Give the extent of all Plasmodium ovale-infected red blood cells.
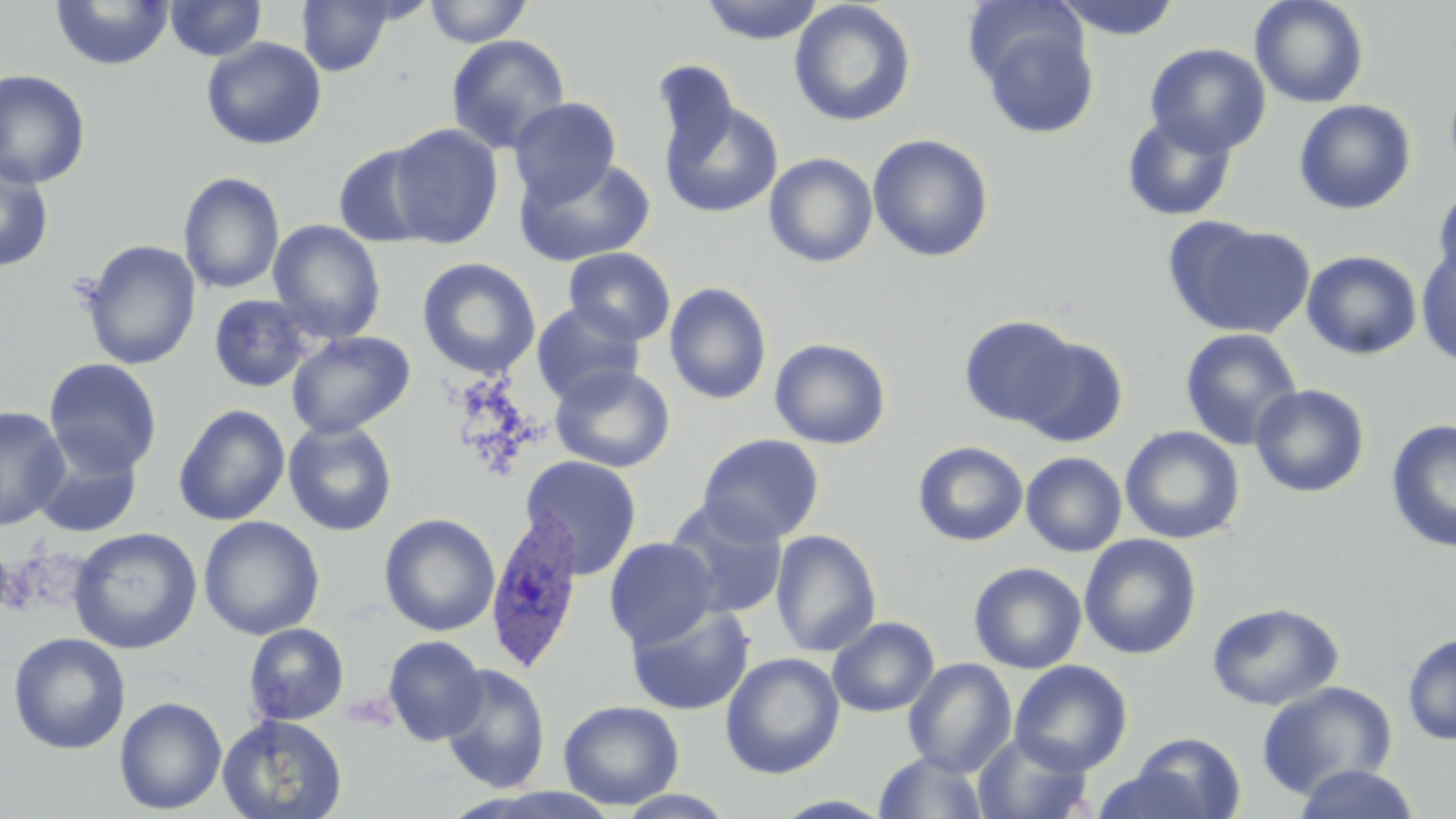
Approximate bounding boxes as [x1, y1, x2, y2] in pixels.
Plasmodium ovale-infected red blood cells: [485, 509, 585, 673].

Summary:
  - Uninfected red blood cell locations: [51, 0, 174, 70], [165, 0, 267, 61], [297, 0, 398, 76], [424, 0, 533, 47], [698, 0, 826, 44], [1052, 0, 1184, 40], [1249, 0, 1370, 109], [789, 1, 916, 127], [976, 16, 1100, 139], [445, 34, 571, 154], [201, 37, 327, 150], [1144, 43, 1272, 156], [650, 58, 742, 169], [0, 69, 92, 189], [508, 97, 621, 205], [659, 98, 783, 219], [1293, 99, 1417, 215], [1121, 113, 1238, 222], [387, 123, 504, 248], [867, 134, 994, 262], [333, 143, 438, 249], [764, 152, 878, 267], [0, 155, 54, 273], [514, 155, 656, 267], [178, 171, 285, 295], [1431, 183, 1456, 297], [1166, 218, 1315, 340], [267, 219, 386, 344], [81, 240, 201, 370], [1416, 246, 1456, 367], [563, 247, 676, 346], [1302, 250, 1422, 360], [417, 258, 541, 378], [664, 282, 772, 405], [208, 294, 314, 393], [531, 301, 645, 405], [958, 315, 1081, 428], [1179, 328, 1303, 450], [286, 330, 415, 439], [1015, 336, 1129, 447], [769, 338, 891, 450], [44, 358, 163, 476], [549, 364, 676, 473], [1249, 383, 1371, 498], [173, 404, 290, 526], [0, 406, 70, 530], [1385, 419, 1456, 553], [283, 420, 398, 537], [1120, 425, 1245, 544], [697, 433, 825, 546], [31, 437, 143, 538], [913, 441, 1028, 546], [1021, 452, 1127, 557], [519, 456, 643, 580], [666, 499, 790, 618], [379, 513, 500, 636], [198, 515, 325, 640], [68, 527, 202, 654], [770, 529, 882, 657], [1079, 534, 1202, 659], [604, 536, 720, 649], [968, 561, 1088, 674], [625, 602, 755, 716], [1207, 602, 1344, 711], [827, 616, 939, 717], [243, 623, 349, 725], [8, 632, 131, 754], [1401, 632, 1456, 746], [382, 635, 488, 746], [720, 652, 845, 779], [903, 658, 1017, 776], [1010, 660, 1133, 775], [440, 663, 551, 793], [1257, 680, 1398, 800], [114, 697, 227, 815], [559, 699, 684, 810], [217, 713, 348, 819], [972, 731, 1095, 819], [1130, 732, 1247, 818], [873, 750, 990, 819], [1293, 763, 1422, 819], [1092, 764, 1211, 819], [614, 789, 738, 818], [770, 794, 897, 818]
  - Slide-level diagnosis: Plasmodium ovale
  - Preparation: thin blood film
  - Modality: light microscopy
  - Magnification: 1000x
  - Stain: May-Grünwald-Giemsa
  - Image size: 1456×819 pixels
  - Field of view: one of a larger specimen